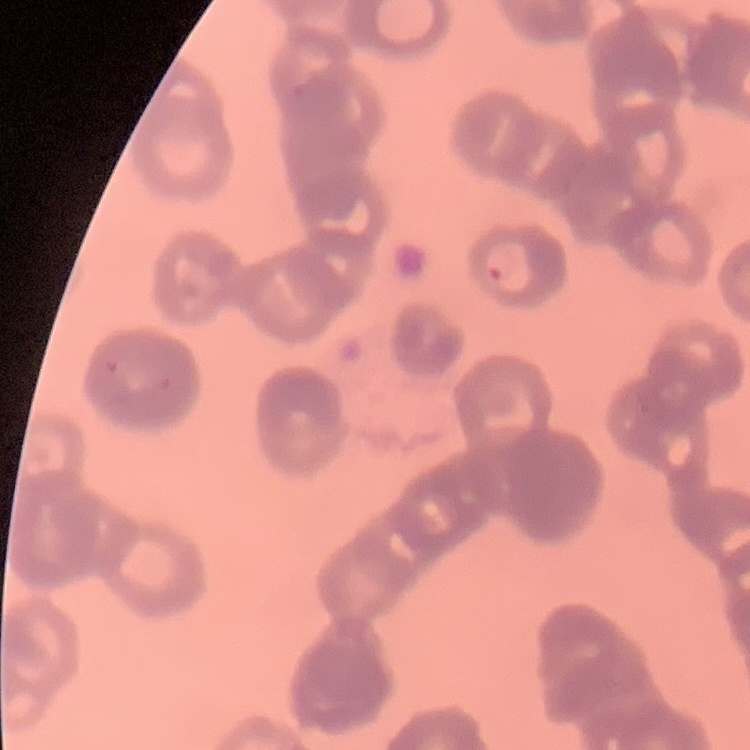
Summary:
  - Red blood cell morphology: rouleaux formation
  - Stain: Field's or Giemsa
  - Image type: square crop of a larger photomicrograph
  - Preparation: thin peripheral smear